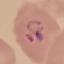
{
  "malaria_status": "parasitized",
  "stain": "Giemsa",
  "preparation": "thin blood film",
  "capture": "smartphone through the microscope eyepiece",
  "image_type": "automatically extracted cell patch, resized to 64 × 64 pixels"
}